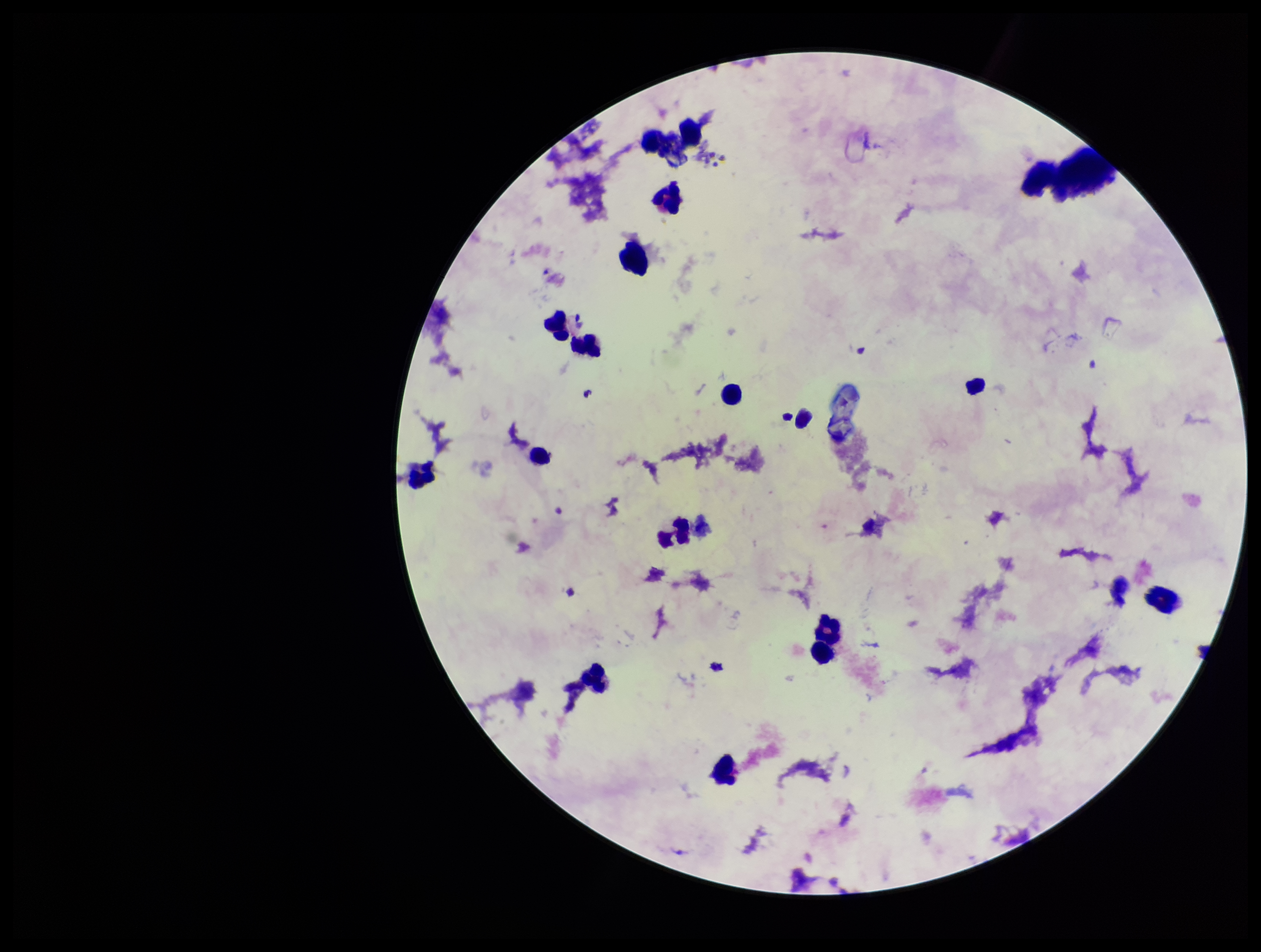

Summary:
  - Patient malaria status: negative
  - Parasite count: 0
  - Leukocyte count: 15
  - Stain: Giemsa
  - Capture: smartphone photograph through the microscope eyepiece
  - Field of view: one from this slide
  - Preparation: thick blood smear
  - Image size: 1261×952 pixels
  - Plasmodium parasites: none identified